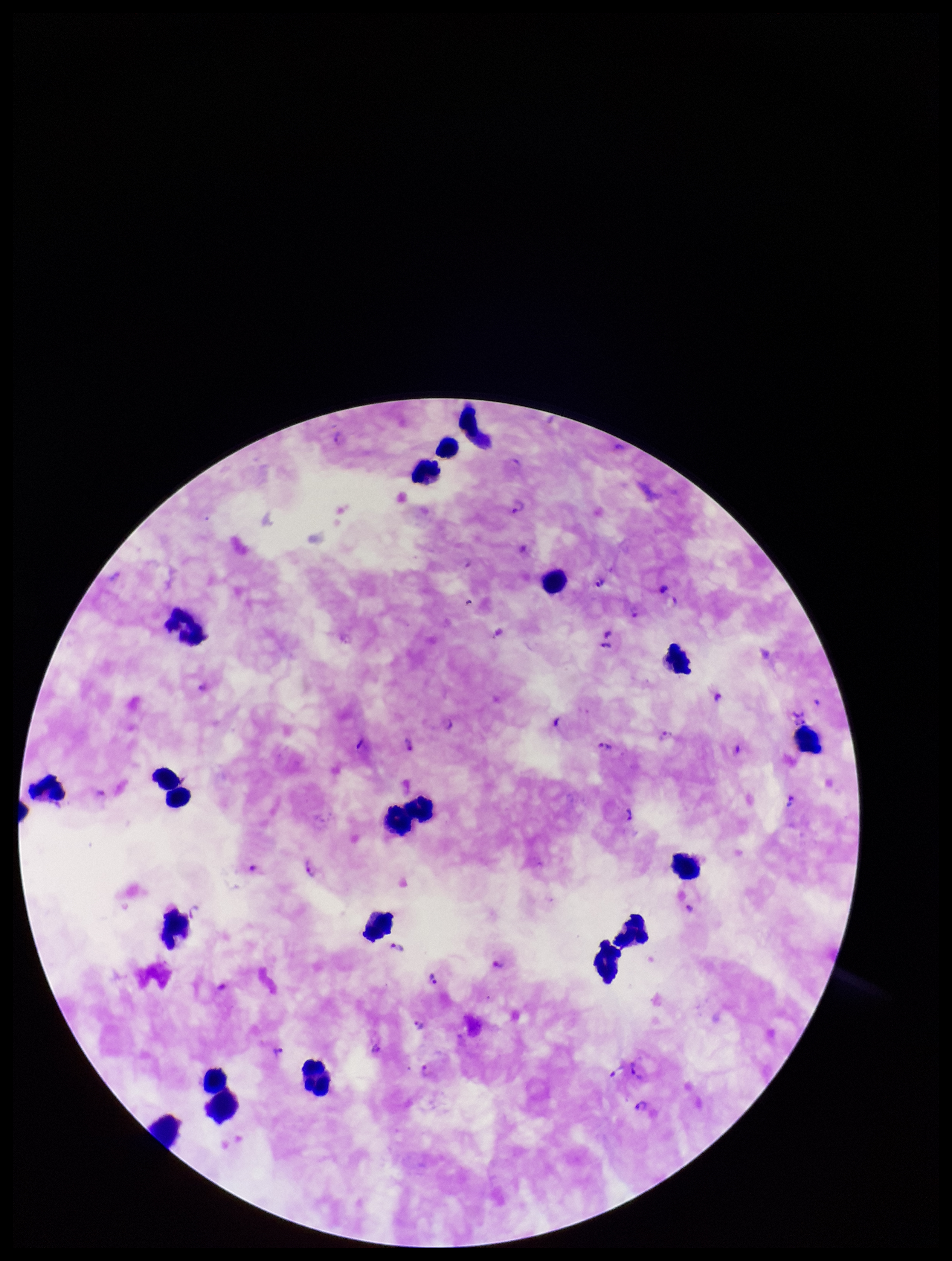
Parasite count: 32. Single field of view. Smartphone photograph taken through the eyepiece of a microscope. Preparation: thick blood smear. Image is 952×1261 pixels. Plasmodium parasites: detected. Patient malaria status: infected. Species reported for this patient: Plasmodium falciparum. Stained with Giemsa. Leukocyte count: 20.